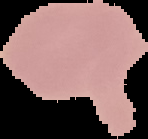
malaria status = uninfected
image size = 148×139 pixels
preparation = thin blood smear
image type = segmented cell region on a black background